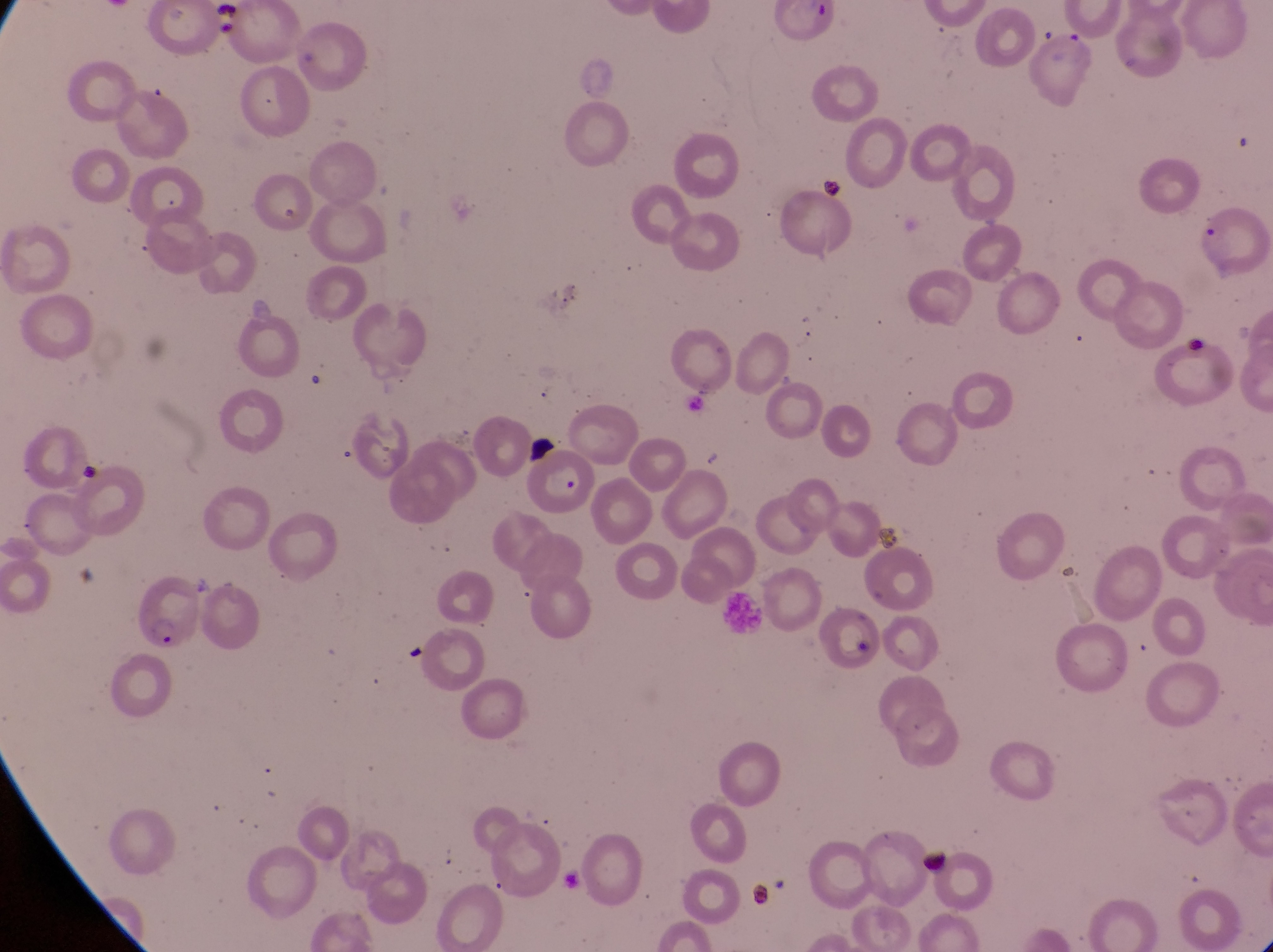
Approximate bounding boxes as (left, top, right, bottom) in pixels. Parasitised red blood cell locations: (530, 447, 592, 519), (130, 587, 200, 661), (814, 612, 886, 674). Leukocyte locations: (717, 586, 777, 632). Artifact (platelet-like body, stain precipitate, or debris) locations: (210, 1, 241, 38), (817, 174, 844, 204), (1181, 317, 1208, 359), (916, 839, 953, 878), (747, 881, 784, 916). Collected in Uganda. Thin blood film. Image is 1273×952 pixels. Magnification of 1000x. Captured by a smartphone held over the eyepiece of an Olympus CX-23 microscope. One field of view.